Name the blood parasite species.
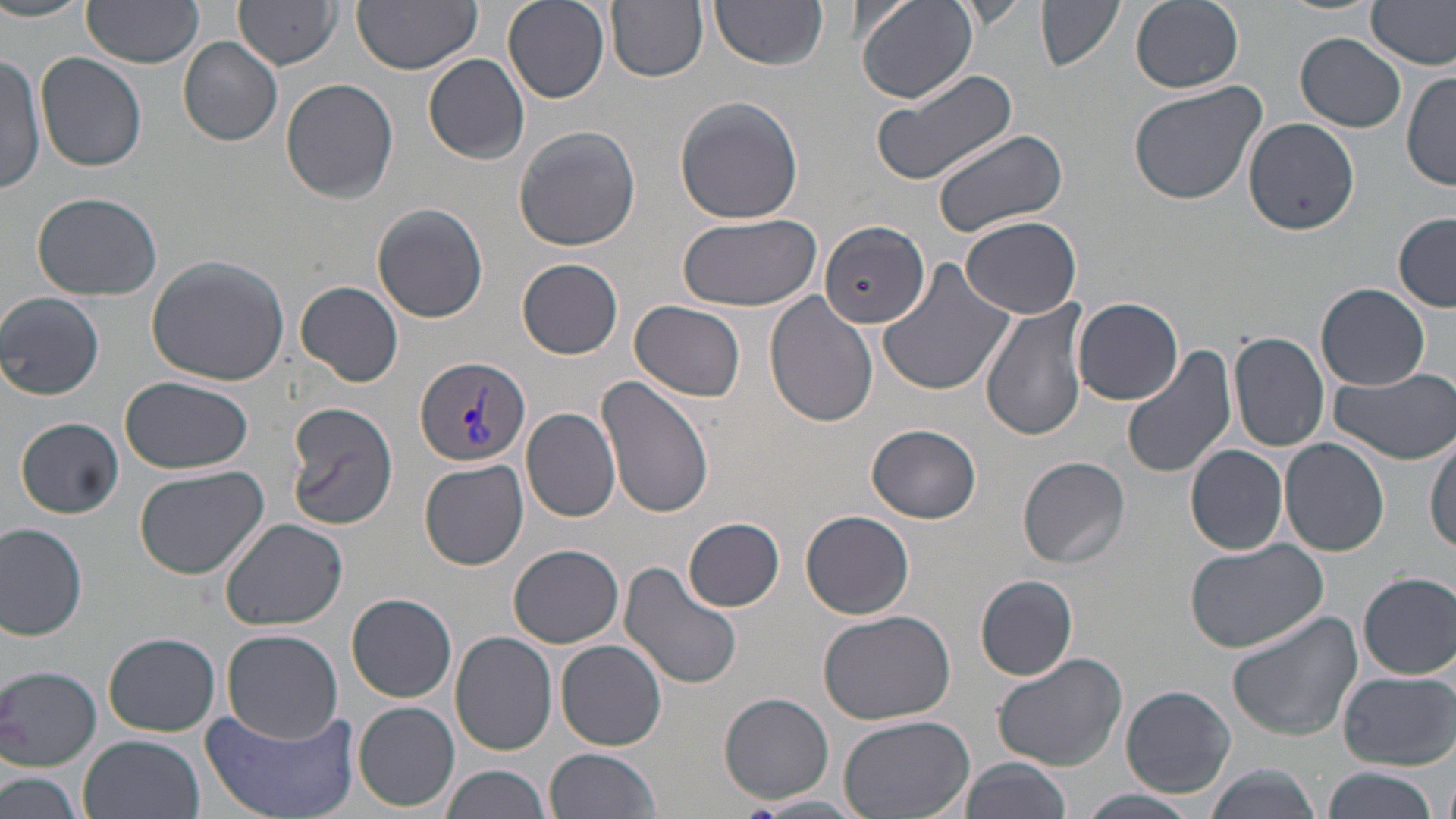
Plasmodium vivax.

preparation = thin blood smear
image size = 1456×819 pixels
field of view = one of a larger specimen
modality = optical microscopy
uninfected red blood cell locations = approximate bounding boxes as (x1, y1, x2, y2) in pixels: (0, 0, 93, 24), (81, 0, 205, 67), (234, 0, 341, 68), (352, 0, 483, 73), (502, 0, 608, 103), (605, 0, 709, 82), (854, 0, 979, 104), (1038, 0, 1126, 73), (1131, 0, 1244, 92), (952, 1, 1031, 29), (711, 2, 825, 70), (1367, 2, 1456, 69), (1296, 33, 1408, 132), (180, 37, 283, 145), (36, 53, 150, 172), (0, 54, 45, 197), (424, 55, 531, 163), (871, 66, 1018, 188), (1403, 69, 1456, 191), (281, 77, 400, 203), (1128, 79, 1269, 207), (673, 96, 804, 224), (1245, 118, 1360, 236), (513, 126, 641, 251), (929, 126, 1070, 240), (32, 192, 165, 300), (372, 203, 489, 323), (1393, 211, 1456, 310), (677, 212, 822, 313), (961, 215, 1082, 318), (823, 219, 928, 323), (145, 255, 292, 386), (518, 258, 623, 359), (877, 258, 1016, 399), (296, 282, 404, 386), (1317, 283, 1430, 391), (764, 291, 880, 428), (0, 292, 104, 400), (1073, 296, 1183, 405), (980, 297, 1091, 441), (631, 299, 746, 402), (1226, 332, 1330, 453), (1123, 344, 1238, 481), (1328, 365, 1456, 464), (596, 375, 715, 519), (121, 376, 253, 475), (285, 401, 400, 531), (522, 405, 620, 524), (16, 418, 125, 518), (866, 423, 982, 524), (1426, 435, 1456, 554), (1280, 437, 1390, 557), (1185, 445, 1289, 555), (1018, 456, 1132, 569), (418, 459, 529, 570), (134, 465, 269, 579), (800, 510, 916, 620), (684, 517, 786, 612), (220, 519, 350, 632), (0, 521, 90, 640), (1184, 539, 1330, 653), (510, 544, 624, 647), (618, 561, 745, 691), (1357, 572, 1456, 680), (975, 574, 1078, 680), (347, 592, 457, 703), (816, 609, 956, 725), (1228, 611, 1362, 741), (222, 630, 344, 745), (449, 630, 557, 755), (105, 632, 220, 736), (556, 639, 668, 751), (991, 650, 1130, 772), (0, 665, 103, 770), (1336, 670, 1453, 768), (1119, 684, 1237, 797), (720, 691, 834, 804), (354, 701, 459, 811), (198, 703, 359, 819), (837, 713, 976, 819), (80, 733, 205, 819), (547, 747, 662, 818), (958, 757, 1071, 819), (440, 764, 550, 819), (1201, 765, 1320, 819), (1319, 766, 1441, 819), (2, 769, 87, 819), (1073, 789, 1205, 818), (756, 793, 867, 815)
magnification = 1000x
stain = May-Grünwald-Giemsa
Plasmodium vivax-infected red blood cell locations = approximate bounding boxes as (x1, y1, x2, y2) in pixels: (414, 355, 531, 466)